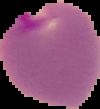
preparation = thin blood smear
image size = 100×109 pixels
image type = cell region segmented out of the field of view; surrounding area masked to black
malaria status = parasitized